Name the parasite shown.
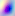
Toxoplasma gondii.

Summary:
  - Modality: micrograph
  - Magnification: 400x